Identify the parasite.
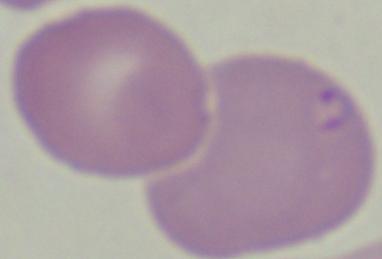

This is Babesia.

Summary:
  - Magnification: 1000x
  - Modality: micrograph